Assess the morphology of the red blood cells.
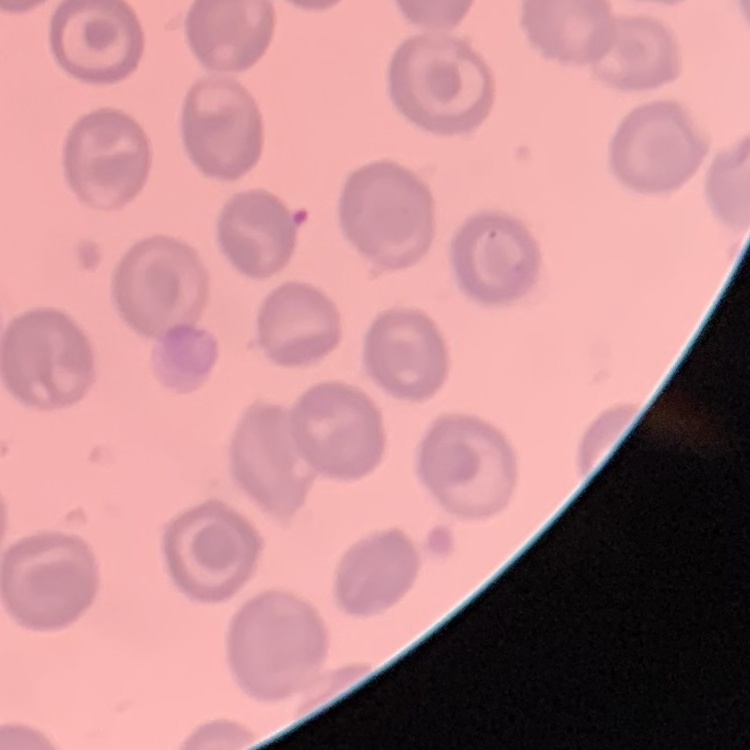
No rouleaux formation.

preparation: thin blood smear
stain: Field's or Giemsa
image_type: square crop of a larger photomicrograph